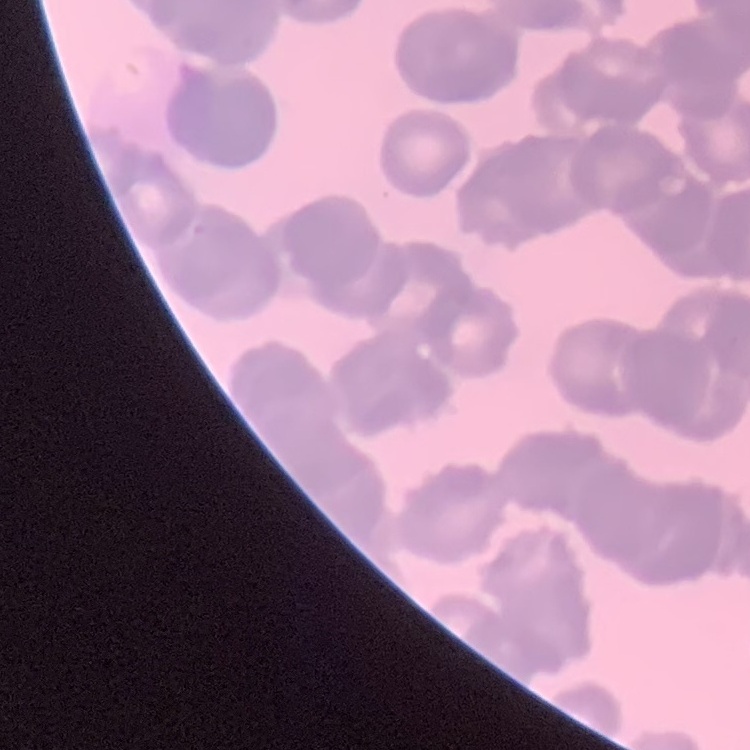

Summary:
  - Red blood cell morphology: rouleaux formation
  - Stain: Field's or Giemsa
  - Preparation: thin blood smear
  - Image type: square crop of a larger photomicrograph